Locate every blood parasite and identify its species.
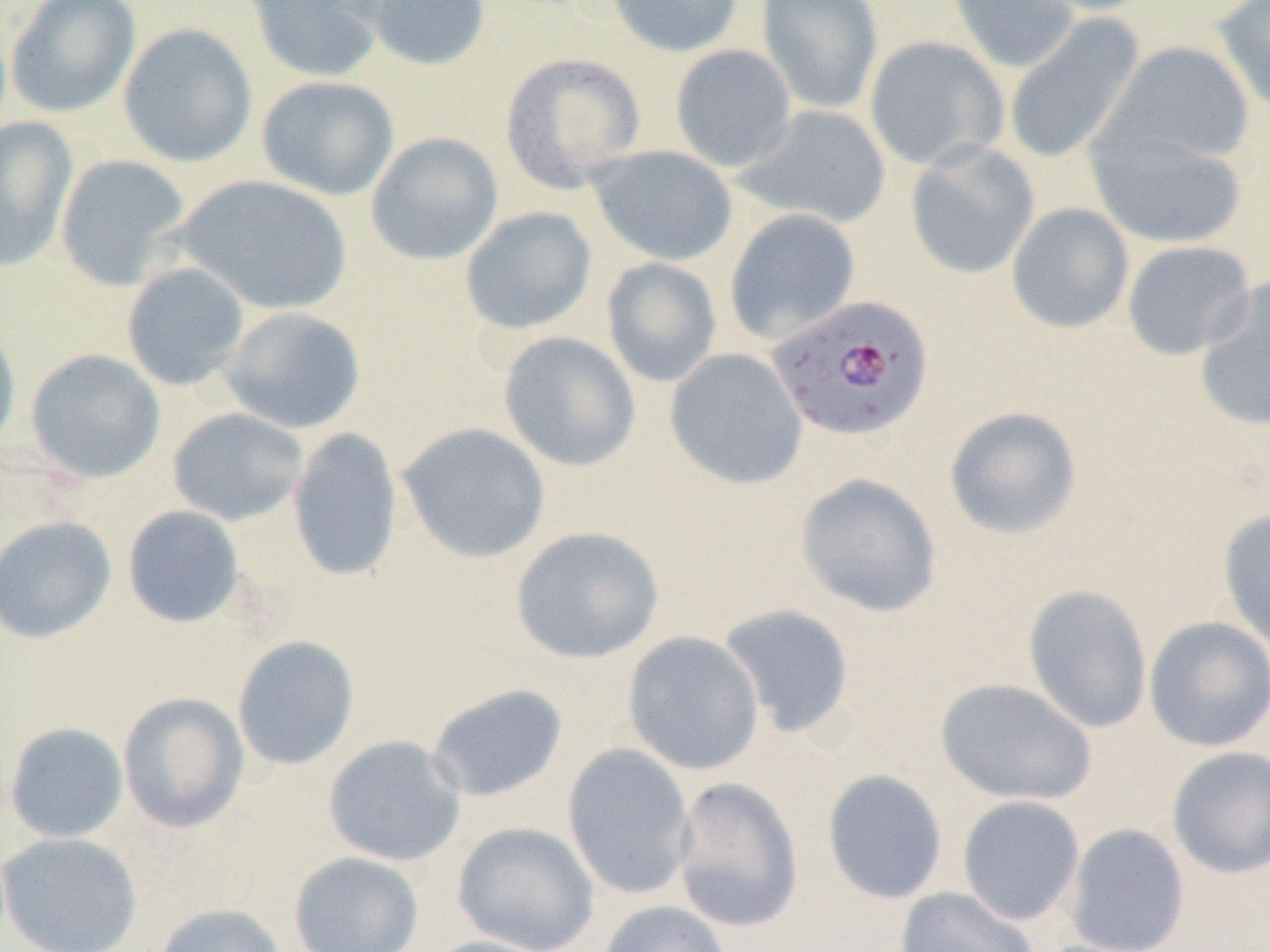
Approximate bounding boxes as [x1, y1, x2, y2] in pixels.
Plasmodium falciparum-infected red blood cells: [765, 293, 935, 444].
No Plasmodium ovale, Plasmodium malariae, Plasmodium vivax, Babesia divergens, or Trypanosoma brucei observed.

Uninfected red blood cell locations: [5, 0, 140, 118], [242, 0, 388, 84], [357, 0, 492, 72], [606, 0, 744, 58], [756, 0, 884, 115], [946, 0, 1081, 73], [1024, 0, 1158, 17], [1213, 0, 1270, 115], [1003, 14, 1145, 164], [117, 22, 258, 169], [864, 36, 1009, 172], [1099, 40, 1256, 167], [669, 44, 797, 174], [499, 51, 646, 192], [256, 75, 399, 201], [735, 104, 892, 229], [0, 115, 78, 272], [1084, 128, 1247, 250], [365, 131, 504, 266], [905, 139, 1040, 280], [586, 144, 738, 266], [55, 154, 191, 292], [171, 174, 352, 317], [1005, 202, 1135, 335], [459, 206, 597, 336], [724, 208, 861, 346], [1121, 239, 1257, 361], [601, 257, 722, 388], [121, 262, 250, 392], [1193, 278, 1270, 432], [220, 305, 365, 434], [0, 318, 22, 459], [498, 331, 641, 472], [664, 347, 808, 490], [25, 348, 166, 483], [943, 405, 1083, 540], [167, 406, 309, 527], [396, 422, 551, 564], [287, 427, 404, 583], [794, 472, 943, 618], [122, 505, 245, 628], [1217, 508, 1270, 650], [0, 516, 116, 645], [509, 525, 665, 665], [1023, 583, 1154, 734], [718, 603, 856, 737], [1143, 616, 1270, 753], [622, 631, 765, 776], [232, 635, 360, 771], [935, 677, 1097, 807], [425, 683, 569, 803], [117, 692, 250, 833], [5, 722, 129, 843], [322, 735, 467, 867], [562, 743, 696, 900], [1166, 745, 1270, 879], [821, 769, 949, 904], [670, 776, 804, 933], [957, 795, 1085, 926], [452, 821, 600, 952], [1064, 822, 1191, 952], [0, 832, 143, 952], [288, 850, 425, 952], [894, 886, 1040, 952], [597, 899, 733, 952], [153, 902, 288, 952], [419, 935, 562, 952]. Slide-level diagnosis: Plasmodium falciparum. Thin blood smear. Light microscopy. 1000x magnification. One field of a larger specimen. Image is 1270×952 pixels.